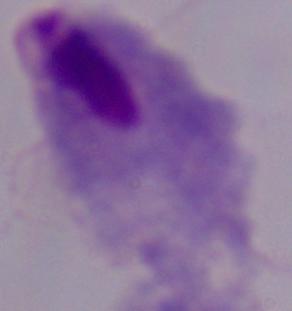

A trichomonad is seen. Captured at 1000x magnification. Photomicrograph.